Comment on the morphology of the erythrocytes.
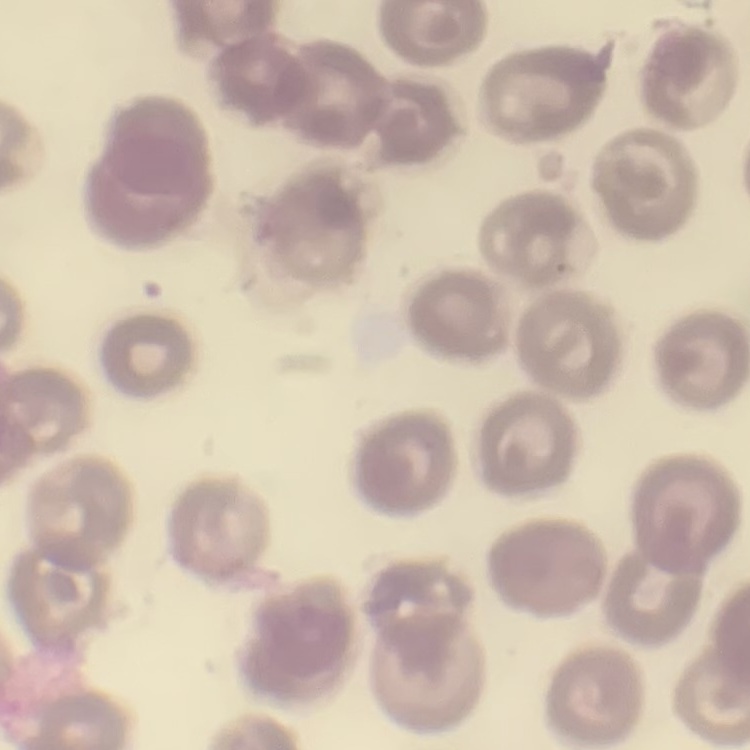
They show no rouleaux formation.

One tile cut from a larger photomicrograph. Field's or Giemsa stain. Thin blood smear.